Locate every Plasmodium parasite and identify its life-cycle stage.
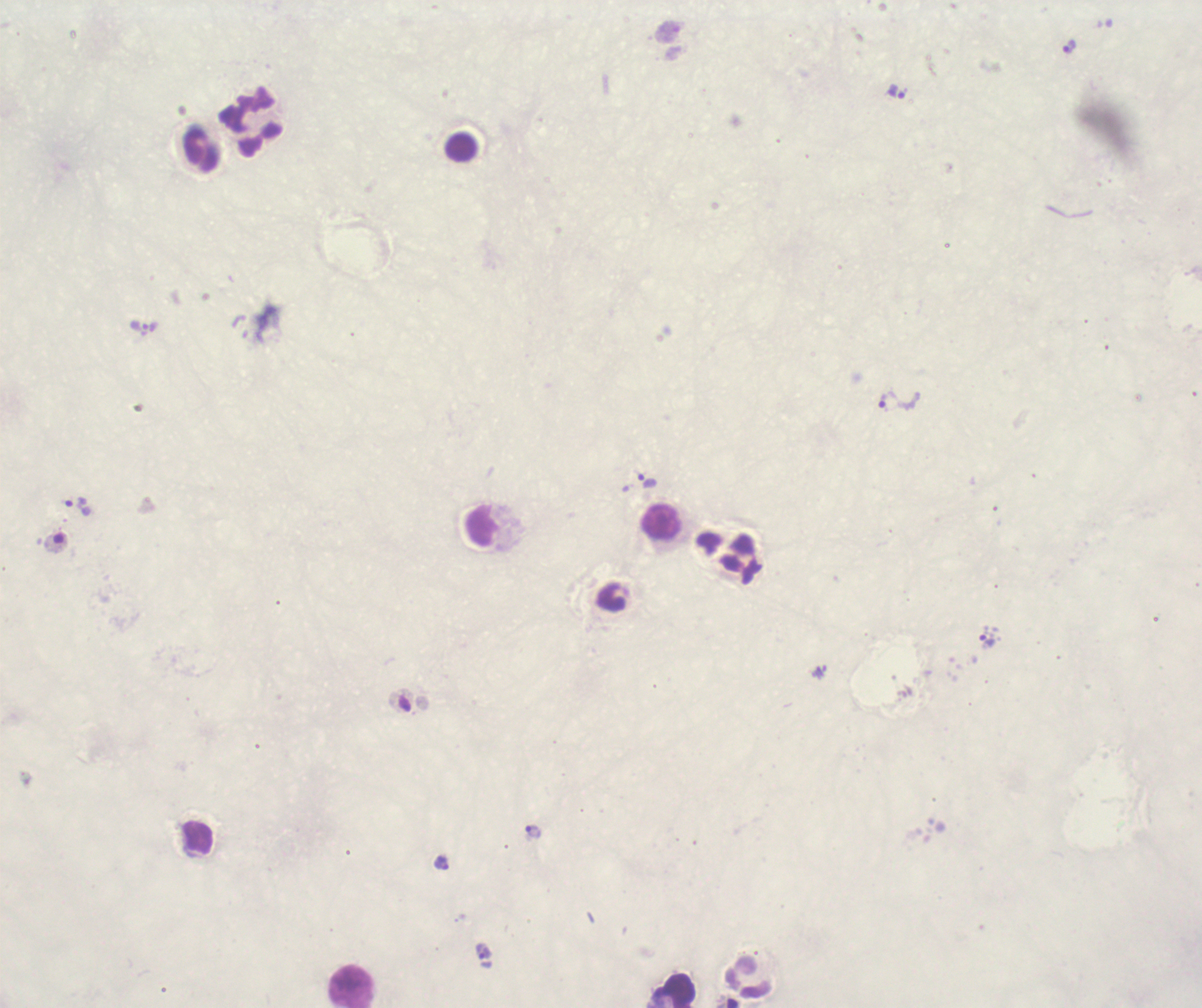

Approximate centers as {x, y} in pixels.
Trophozoites: {1070, 47}, {897, 91}, {144, 328}, {898, 401}, {647, 482}, {79, 507}, {987, 639}, {534, 832}, {441, 863}, {483, 952}.
No schizont or gametocyte forms observed.

Approximate centers as {x, y} in pixels.
Summary:
  - Leukocyte locations: {251, 122}, {201, 149}, {661, 522}, {482, 525}, {742, 560}, {197, 838}, {749, 976}, {351, 987}
  - Preparation: thick blood smear
  - Image size: 1202×1008 pixels
  - Context: previously used in a real diagnosis
  - Field of view: one from this slide
  - Magnification: 100x
  - Stain: Romanowsky
  - Coloration quality: bad
  - Background quality: unsatisfactory